Rate the background quality.
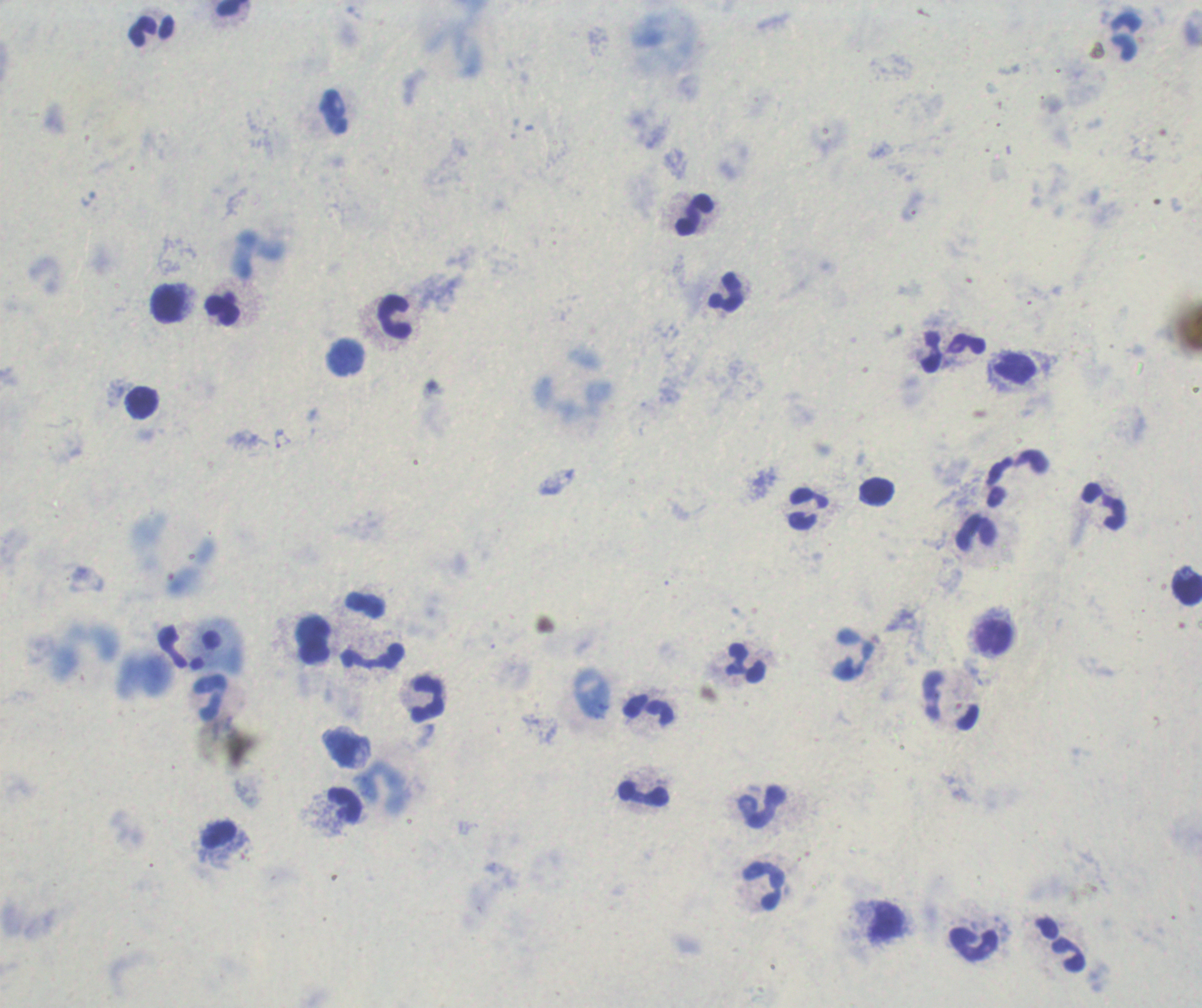

Unsatisfactory.

Approximate centers as (x, y) in pixels. Leukocyte locations: (151, 30), (1125, 37), (695, 215), (726, 293), (168, 303), (221, 309), (394, 316), (966, 345), (933, 353), (345, 357), (1017, 368), (141, 402), (1017, 479), (1104, 507), (808, 509), (976, 532), (1187, 589), (365, 605), (994, 636), (313, 639), (854, 654), (371, 656), (747, 663), (211, 698), (428, 699), (952, 699), (649, 709), (644, 794), (344, 803), (762, 808), (220, 835), (763, 885), (884, 920), (975, 945), (1069, 955). Previously used in a real diagnosis. Image is 1202×1008 pixels. Captured at 100x magnification. Result: negative for Plasmodium parasites. Single field of view. Romanowsky-stained preparation. Thick blood smear.